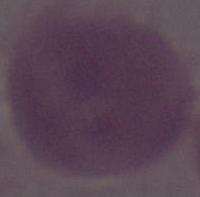 1000x magnification. A red blood cell is seen. Photomicrograph.